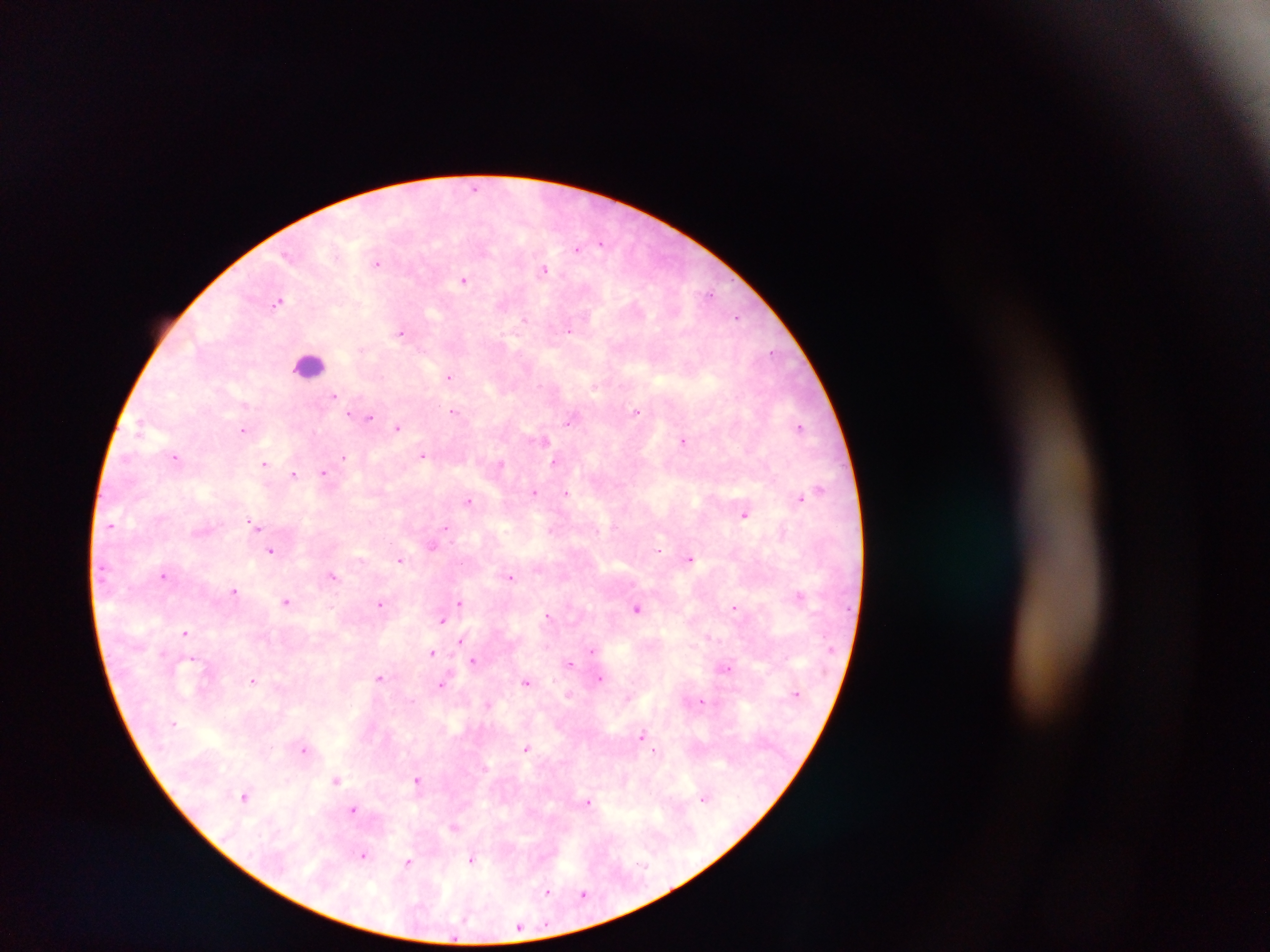 Approximate centers as {x, y} in pixels. Plasmodium parasite locations: {475, 187}, {602, 243}, {578, 248}, {287, 254}, {378, 263}, {543, 269}, {463, 280}, {710, 295}, {279, 300}, {737, 317}, {524, 320}, {569, 330}, {401, 331}, {772, 351}, {450, 376}, {334, 395}, {245, 405}, {454, 412}, {636, 412}, {349, 414}, {370, 418}, {569, 421}, {800, 427}, {398, 428}, {243, 429}, {683, 440}, {544, 441}, {423, 456}, {344, 457}, {176, 458}, {554, 462}, {264, 463}, {501, 464}, {324, 473}, {294, 474}, {820, 489}, {533, 492}, {565, 492}, {801, 497}, {469, 501}, {745, 514}, {253, 523}, {110, 526}, {446, 528}, {433, 546}, {659, 549}, {271, 551}, {689, 558}, {399, 561}, {333, 575}, {164, 576}, {510, 577}, {234, 590}, {800, 595}, {286, 602}, {459, 602}, {380, 604}, {637, 608}, {734, 608}, {547, 615}, {442, 620}, {185, 632}, {461, 641}, {591, 651}, {432, 653}, {193, 659}, {473, 661}, {569, 662}, {726, 668}, {380, 677}, {600, 678}, {252, 680}, {526, 681}, {442, 685}, {570, 694}, {701, 701}, {488, 704}, {642, 735}, {527, 748}, {304, 750}, {655, 751}, {418, 780}, {336, 781}, {245, 796}, {703, 798}, {588, 802}, {353, 809}, {453, 827}, {363, 855}, {472, 860}, {408, 863}, {547, 892}, {583, 894}. Leukocyte locations: {308, 364}. One field of view. Sample from Ghana. Photographed through a microscope with a mobile-phone camera. Image is 1270×952 pixels. Thick blood film.